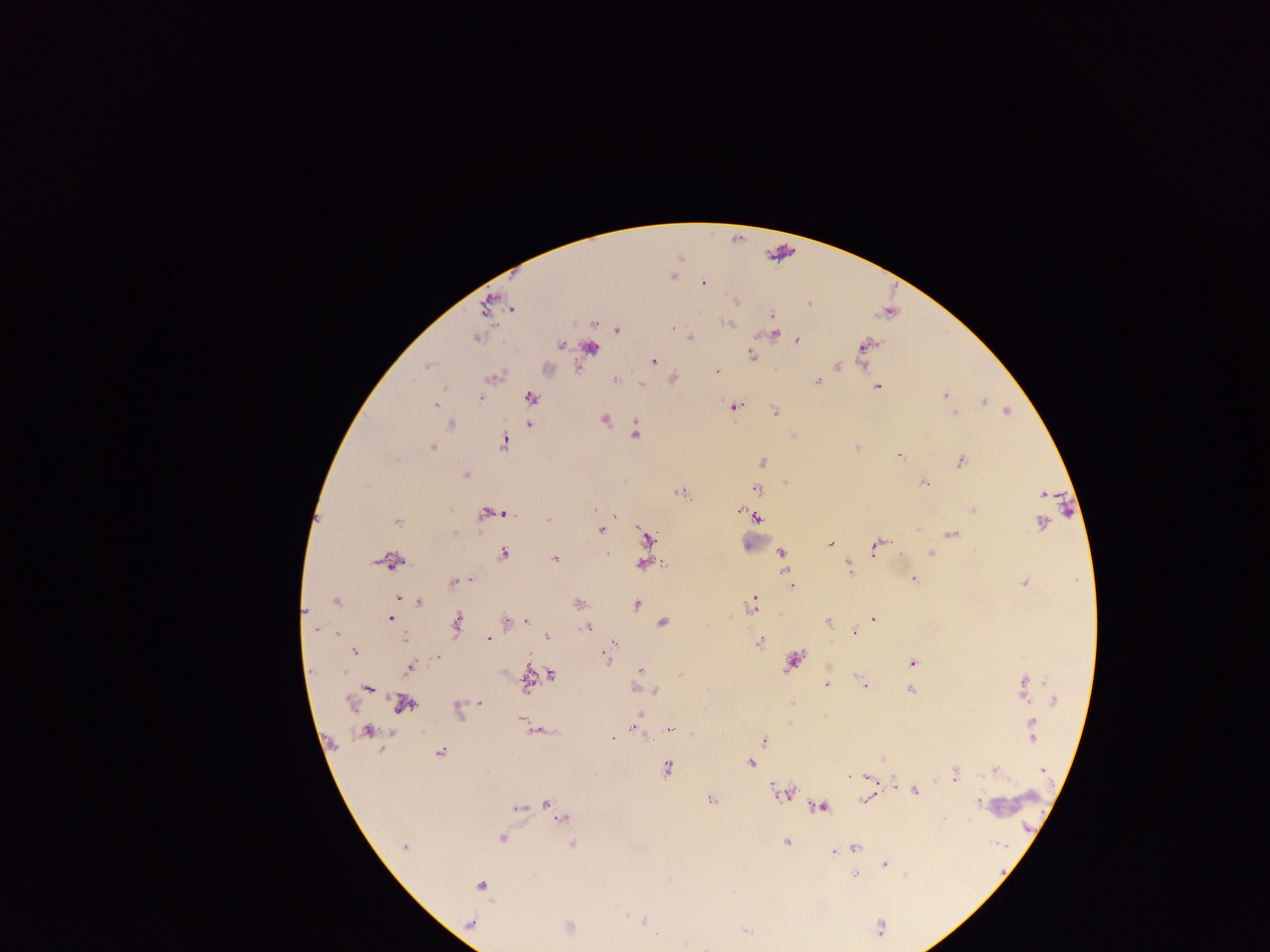

Approximate centers as [x, y] in pixels.
Summary:
  - Plasmodium parasite locations: [672, 275], [703, 282], [734, 301], [808, 304], [486, 305], [511, 308], [771, 316], [594, 323], [728, 323], [671, 328], [617, 330], [772, 334], [476, 338], [690, 338], [796, 340], [866, 344], [560, 345], [590, 347], [751, 354], [653, 361], [862, 363], [427, 365], [837, 366], [576, 367], [546, 369], [716, 371], [492, 377], [614, 378], [673, 379], [818, 381], [641, 384], [877, 386], [945, 395], [480, 397], [530, 397], [984, 401], [436, 405], [734, 405], [1006, 411], [774, 412], [954, 414], [605, 419], [528, 423], [449, 424], [635, 431], [793, 435], [503, 441], [431, 447], [857, 447], [899, 455], [961, 460], [763, 462], [465, 474], [784, 481], [922, 482], [756, 488], [681, 492], [1043, 494], [595, 510], [740, 510], [973, 510], [503, 512], [486, 513], [495, 513], [757, 517], [547, 518], [397, 520], [1042, 522], [601, 530], [950, 533], [646, 538], [830, 544], [877, 544], [937, 547], [931, 551], [781, 552], [503, 553], [554, 559], [390, 560], [848, 560], [643, 563], [663, 564], [849, 569], [913, 578], [471, 579], [453, 581], [1025, 582], [791, 584], [398, 598], [336, 601], [419, 602], [578, 603], [751, 604], [636, 605], [306, 611], [391, 618], [873, 619], [528, 621], [828, 621], [457, 622], [505, 622], [662, 622], [588, 627], [316, 629], [857, 629], [853, 632], [546, 636], [487, 639], [614, 642], [758, 642], [353, 651], [604, 655], [438, 656], [793, 660], [911, 663], [410, 667], [639, 670], [551, 674], [682, 674], [527, 680], [826, 684], [864, 684], [1023, 687], [368, 688], [637, 689], [911, 689], [654, 691], [1053, 701], [349, 703], [479, 703], [402, 704], [456, 709], [640, 715], [521, 718], [635, 724], [672, 728], [640, 729], [537, 731], [367, 732], [1031, 733], [613, 739], [764, 740], [440, 752], [883, 758], [750, 763], [667, 769], [1043, 770], [995, 771], [955, 774], [850, 776], [868, 777], [774, 784], [893, 784], [915, 791], [787, 793], [867, 799], [710, 800], [978, 801], [546, 804], [532, 806], [820, 807], [517, 808], [555, 812], [562, 819], [501, 838], [786, 842], [572, 843], [405, 846], [854, 847], [834, 851], [884, 863], [854, 875], [481, 885], [644, 921], [470, 923], [568, 927], [746, 930]
  - Image size: 1270×952 pixels
  - Preparation: thick blood smear
  - Field of view: single
  - Country: Ghana
  - Capture: mobile-phone photograph through a microscope